Locate every blood parasite and identify its species.
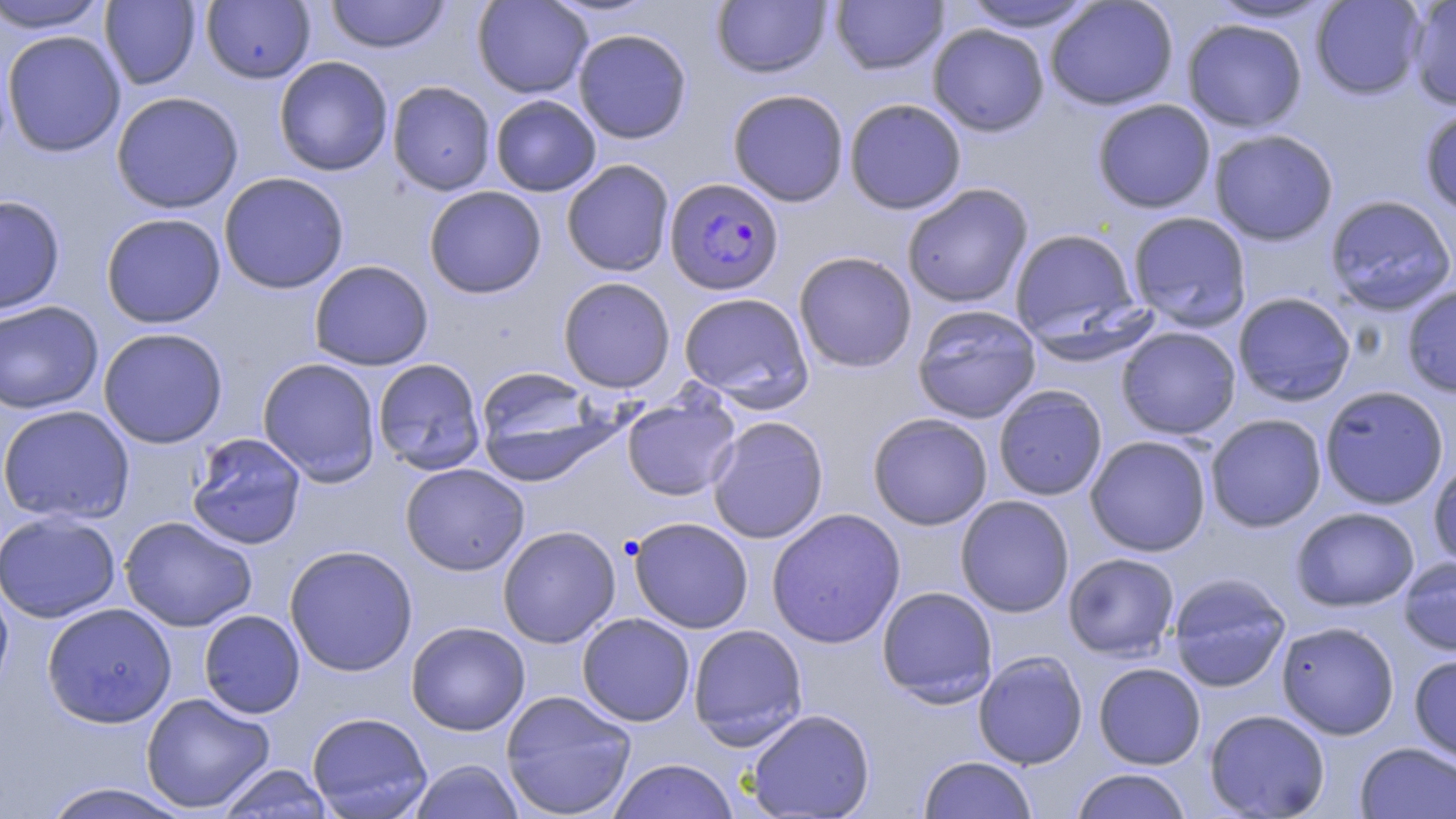

Approximate bounding boxes as (x1,y1)-(x2,y2) corner pairs in pixels.
Plasmodium falciparum-infected red blood cells: (664,177)-(784,295).
No Plasmodium ovale, Plasmodium malariae, Plasmodium vivax, Babesia divergens, or Trypanosoma brucei observed.

Summary:
  - Uninfected red blood cell locations: (1,0)-(111,34), (325,0)-(451,53), (472,0)-(593,98), (830,0)-(948,75), (1204,0)-(1339,25), (1310,0)-(1427,100), (1406,0)-(1456,110), (100,1)-(202,89), (201,1)-(316,84), (711,1)-(832,78), (959,1)-(1099,33), (1045,1)-(1179,111), (1182,18)-(1307,133), (927,23)-(1050,136), (573,28)-(692,144), (1,30)-(126,157), (274,56)-(393,176), (386,81)-(496,195), (727,88)-(850,207), (111,91)-(244,214), (490,94)-(602,196), (844,98)-(967,214), (1091,98)-(1216,213), (1419,104)-(1456,218), (1208,128)-(1339,246), (561,159)-(675,277), (218,172)-(350,295), (902,184)-(1033,308), (424,186)-(546,299), (0,194)-(66,316), (1324,194)-(1455,315), (1126,211)-(1252,331), (100,212)-(226,329), (1008,227)-(1144,349), (793,251)-(918,373), (308,260)-(434,371), (558,276)-(676,393), (1401,283)-(1456,398), (1232,291)-(1357,407), (678,292)-(814,410), (0,301)-(104,414), (912,304)-(1042,424), (1116,326)-(1241,439), (97,327)-(228,449), (257,357)-(382,486), (372,358)-(486,475), (475,366)-(609,482), (1319,385)-(1449,509), (993,386)-(1108,501), (621,393)-(741,501), (0,405)-(135,524), (867,412)-(993,530), (1205,413)-(1327,532), (707,415)-(829,544), (186,433)-(308,550), (1084,435)-(1212,557), (1428,459)-(1456,571), (400,463)-(530,576), (955,495)-(1075,618), (1291,506)-(1420,612), (766,508)-(906,649), (0,511)-(121,623), (119,516)-(258,632), (628,517)-(754,633), (497,525)-(620,648), (283,544)-(418,677), (1063,553)-(1180,661), (1397,556)-(1456,656), (1166,573)-(1291,692), (0,576)-(14,702), (876,586)-(998,707), (42,602)-(177,727), (198,609)-(306,719), (576,613)-(695,726), (406,621)-(530,736), (1276,621)-(1400,739), (687,624)-(808,748), (973,650)-(1088,769), (1408,653)-(1456,764), (1093,662)-(1206,769), (500,690)-(637,818), (141,692)-(276,813), (746,708)-(876,818), (1204,708)-(1331,818), (306,711)-(434,819), (1355,742)-(1456,818), (918,755)-(1038,819), (608,758)-(739,819), (409,760)-(524,819), (216,764)-(334,818), (1071,768)-(1193,818), (38,782)-(195,819)
  - Slide-level diagnosis: Plasmodium falciparum
  - Stain: May-Grünwald-Giemsa
  - Magnification: 1000x
  - Modality: light microscopy
  - Image size: 1456×819 pixels
  - Field of view: single
  - Preparation: thin blood smear